Report the malaria status of this cell.
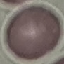

It is uninfected.

Summary:
  - Capture: smartphone camera at the microscope eyepiece
  - Preparation: thin blood film
  - Image type: cell patch, automatically extracted from a larger field of view and resized to 64 × 64 pixels
  - Stain: Giemsa